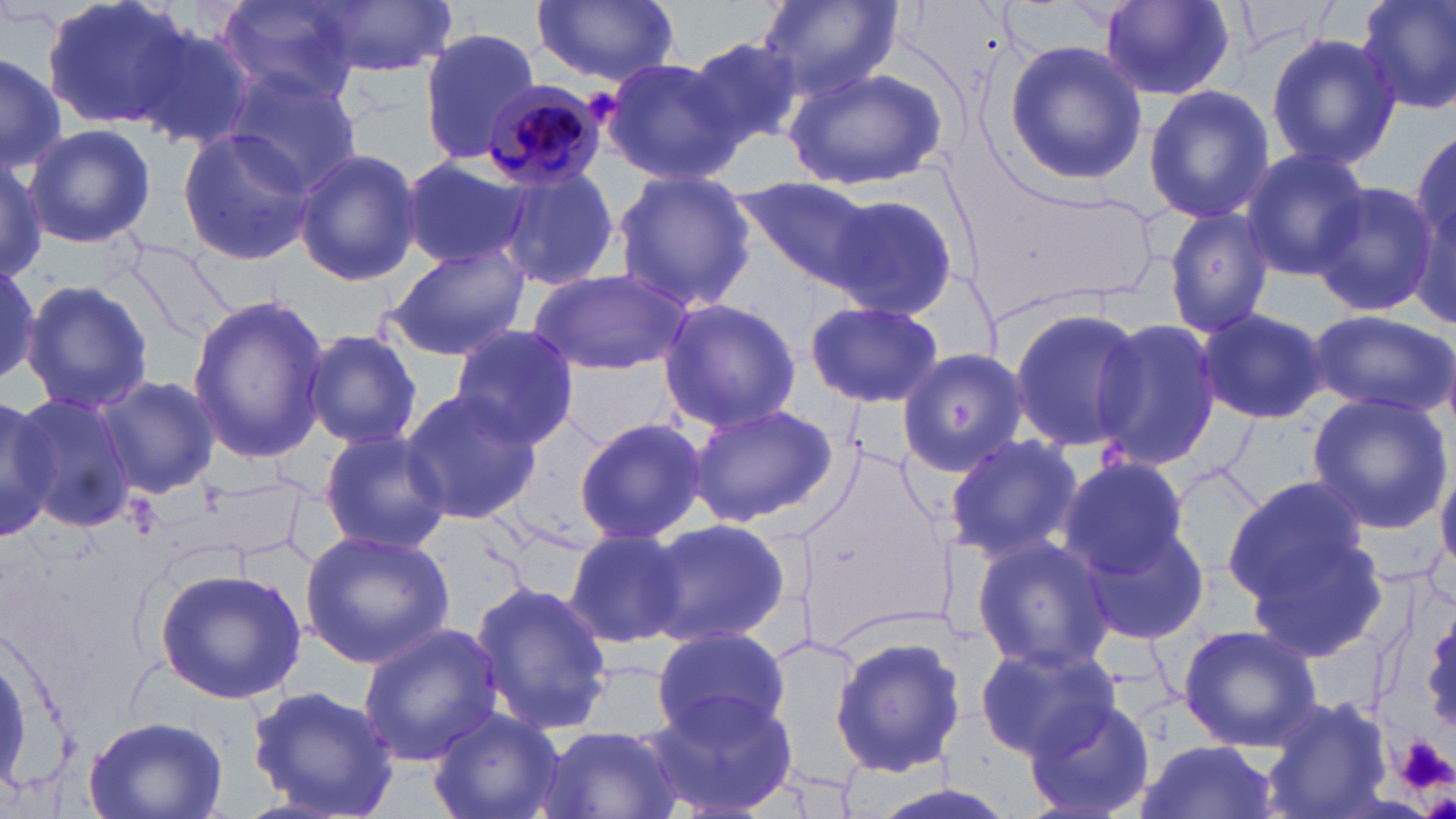 Approximate bounding boxes as [x1, y1, x2, y2] in pixels. Uninfected red blood cell locations: [42, 0, 201, 133], [217, 0, 361, 104], [532, 0, 681, 87], [756, 0, 903, 99], [1353, 0, 1456, 116], [312, 1, 454, 78], [1101, 2, 1238, 101], [130, 19, 261, 150], [419, 25, 543, 165], [1265, 31, 1401, 171], [685, 35, 809, 152], [1003, 40, 1146, 185], [0, 49, 66, 170], [600, 56, 743, 184], [784, 64, 949, 190], [218, 66, 364, 198], [1143, 86, 1275, 225], [1410, 122, 1454, 291], [24, 124, 156, 249], [177, 125, 316, 268], [1237, 147, 1369, 281], [293, 149, 422, 286], [0, 152, 48, 284], [398, 154, 532, 272], [494, 165, 622, 291], [611, 171, 755, 314], [738, 177, 893, 294], [1312, 181, 1439, 318], [820, 189, 961, 321], [1162, 206, 1277, 339], [1173, 220, 1307, 404], [383, 244, 530, 360], [0, 256, 47, 391], [529, 269, 694, 376], [21, 278, 153, 415], [186, 296, 333, 460], [655, 298, 803, 432], [805, 300, 944, 409], [1195, 305, 1328, 424], [1006, 306, 1146, 454], [1305, 309, 1456, 418], [1093, 316, 1221, 468], [448, 325, 583, 451], [301, 329, 428, 450], [896, 347, 1031, 477], [95, 374, 220, 500], [401, 388, 542, 524], [13, 390, 141, 535], [1306, 393, 1453, 534], [0, 399, 72, 535], [685, 402, 837, 529], [574, 416, 706, 543], [319, 430, 453, 556], [943, 432, 1082, 564], [1436, 456, 1456, 569], [1056, 458, 1189, 577], [1173, 464, 1265, 582], [1223, 476, 1371, 605], [204, 480, 302, 562], [642, 517, 790, 649], [1071, 518, 1210, 645], [563, 526, 690, 648], [299, 528, 455, 667], [1246, 531, 1391, 661], [970, 535, 1116, 673], [154, 565, 307, 704], [471, 580, 616, 738], [355, 622, 503, 766], [649, 625, 792, 744], [1177, 625, 1322, 752], [830, 633, 966, 778], [972, 639, 1119, 759], [244, 683, 404, 818], [646, 690, 798, 816], [1262, 695, 1390, 819], [1022, 696, 1159, 819], [426, 707, 568, 819], [83, 713, 228, 818], [537, 725, 683, 819], [1134, 740, 1277, 819]. Plasmodium malariae-infected red blood cell locations: [483, 80, 608, 193]. Platelet locations: [1396, 735, 1456, 793]. Slide-level diagnosis: Plasmodium malariae. Optical microscopy. One field of a larger specimen. Thin blood film. May-Grünwald-Giemsa-stained preparation. Image is 1456×819 pixels. Captured at 1000x magnification.